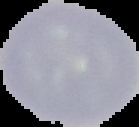

{
  "image_size": "139×127 pixels",
  "preparation": "thin blood smear",
  "image_type": "cell region segmented out of the field of view; surrounding area masked to black",
  "result": "no Plasmodium parasites seen"
}